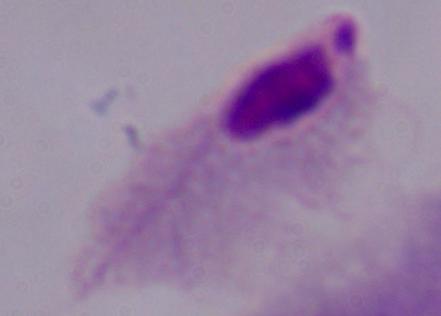

Captured at 1000x magnification. Micrograph. A trichomonad is seen.